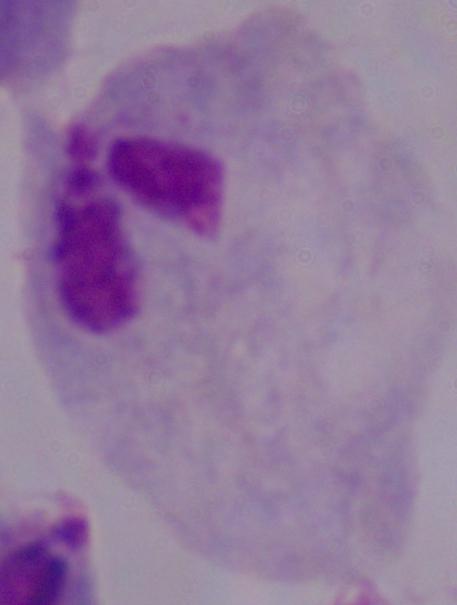 Captured at 1000x magnification. A trichomonad is shown. Photomicrograph.